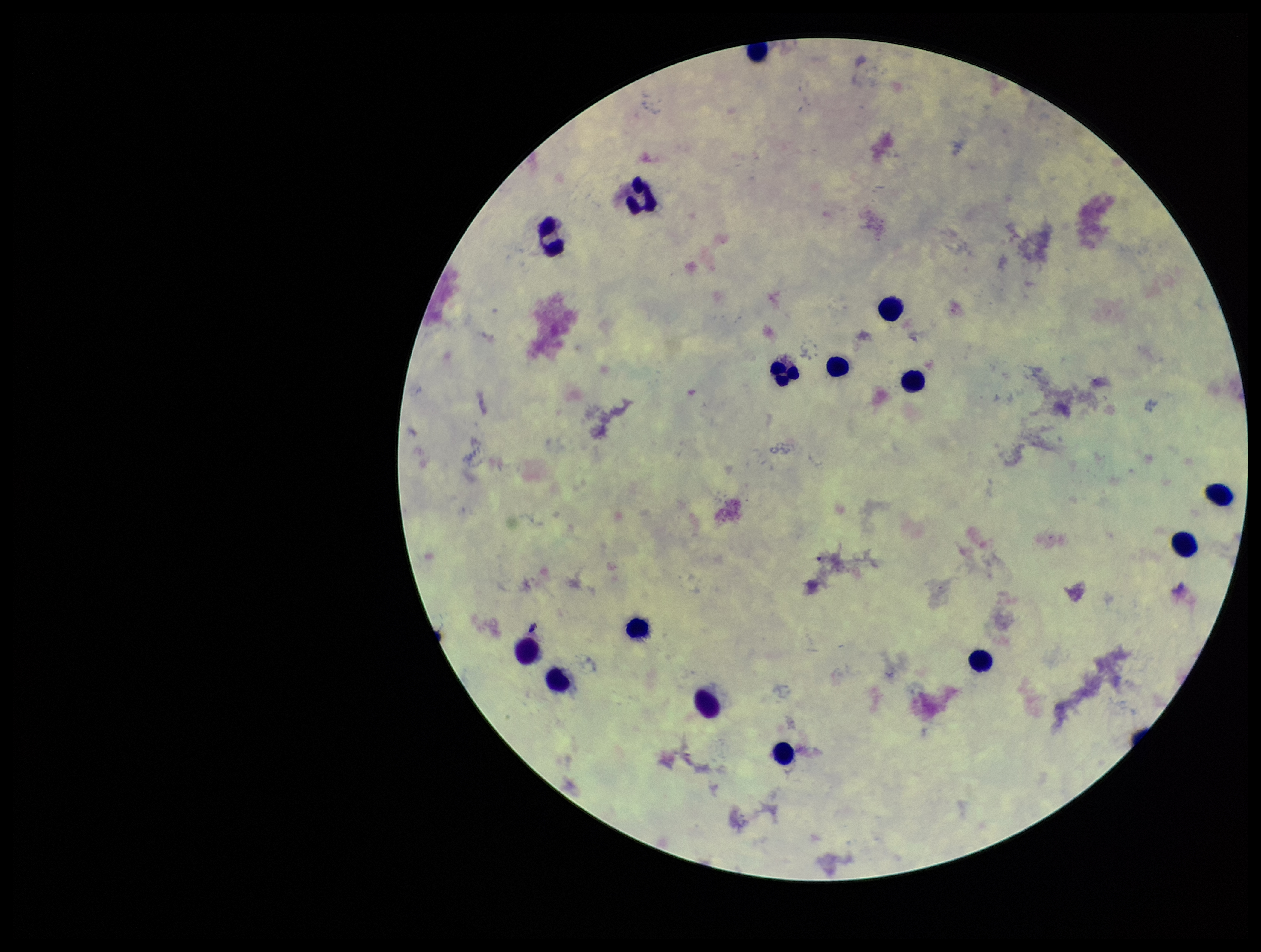
Summary:
  - Plasmodium parasites: none identified
  - Stain: Giemsa
  - Field of view: single
  - Preparation: thick smear
  - Parasite count: 0
  - Capture: smartphone photograph through the microscope eyepiece
  - Leukocyte count: 15
  - Image size: 1261×952 pixels
  - Patient malaria status: negative